Outline each uninfected red blood cell.
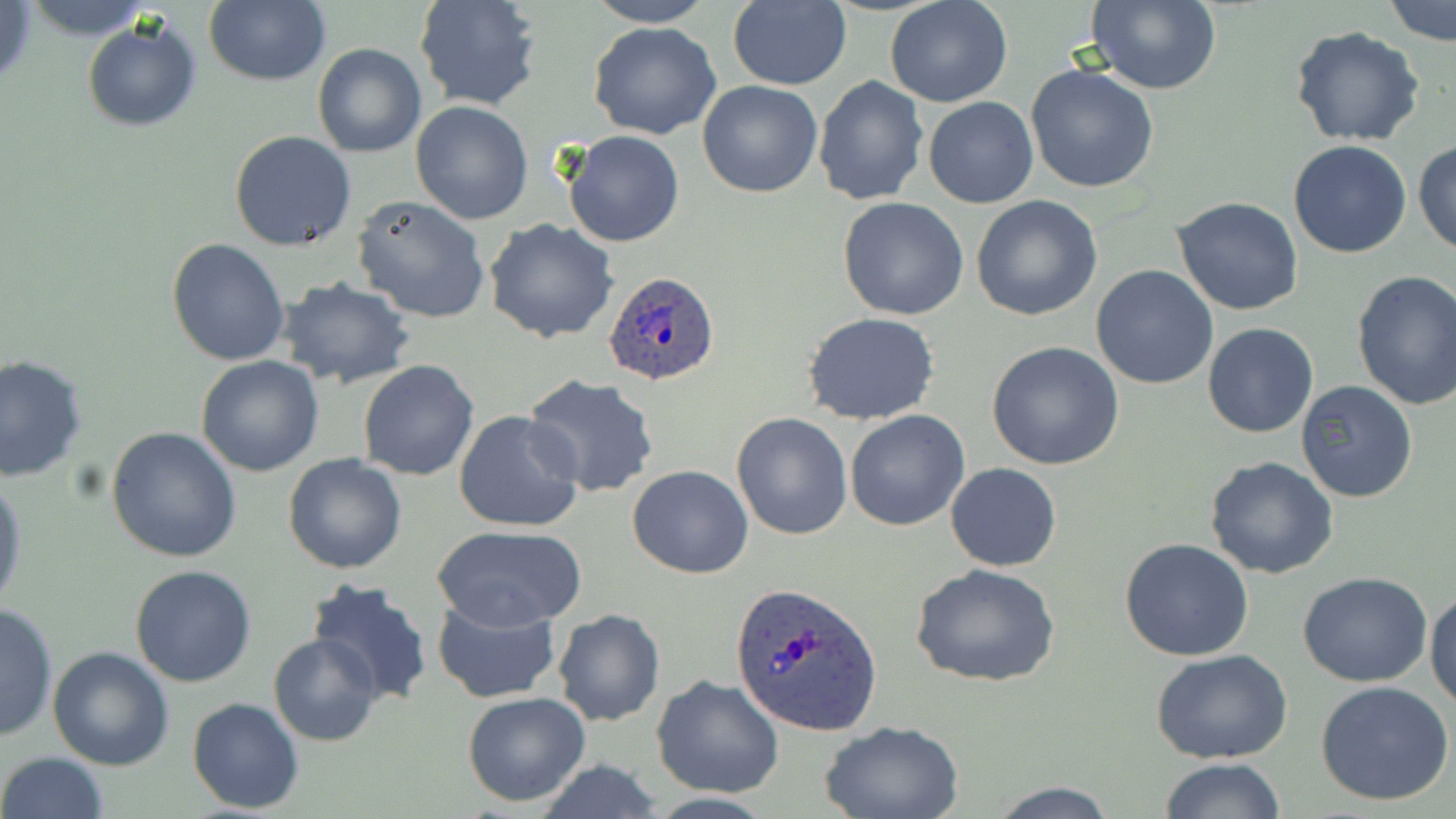
Approximate bounding boxes as (x1,y1)-(x2,y2) corner pairs in pixels.
Uninfected red blood cells: (204,0)-(330,87), (414,0)-(545,113), (584,0)-(716,26), (886,0)-(1013,107), (1384,0)-(1456,46), (725,1)-(852,89), (1086,1)-(1223,94), (0,2)-(38,90), (80,18)-(202,132), (587,20)-(722,140), (1289,26)-(1428,149), (312,43)-(426,158), (1025,63)-(1160,194), (813,74)-(928,207), (697,81)-(824,198), (922,96)-(1038,209), (409,100)-(533,224), (228,129)-(356,251), (563,129)-(686,247), (1288,140)-(1413,258), (1413,140)-(1456,257), (352,195)-(491,324), (971,195)-(1103,321), (837,197)-(969,321), (1172,197)-(1304,316), (485,219)-(619,342), (167,239)-(290,366), (1091,265)-(1219,390), (1351,270)-(1456,412), (276,275)-(416,390), (803,313)-(941,425), (1202,322)-(1319,438), (986,341)-(1127,470), (0,354)-(89,483), (196,355)-(324,476), (357,359)-(481,480), (523,375)-(659,497), (1295,379)-(1419,502), (454,410)-(584,533), (844,410)-(970,531), (731,412)-(853,540), (106,426)-(241,563), (283,453)-(409,574), (1204,455)-(1339,579), (945,464)-(1061,571), (628,465)-(754,578), (0,472)-(26,615), (433,524)-(587,630), (1120,536)-(1254,661), (910,562)-(1061,688), (130,563)-(257,686), (1297,571)-(1433,687), (303,576)-(434,706), (1426,587)-(1456,712), (430,595)-(562,704), (0,601)-(58,743), (553,609)-(666,727), (268,633)-(382,746), (48,645)-(175,770), (1151,648)-(1294,763), (652,674)-(784,798), (1314,680)-(1456,807), (463,692)-(591,807), (188,697)-(305,814), (821,720)-(964,819), (0,751)-(109,819), (1160,756)-(1287,819), (530,760)-(669,819), (982,780)-(1121,816).

Plasmodium ovale-infected red blood cell locations: (603,271)-(723,385), (729,582)-(882,735). Slide-level diagnosis: Plasmodium ovale. 1000x magnification. Optical microscopy. Image is 1456×819 pixels. One field of a larger specimen. Thin blood smear. May-Grünwald-Giemsa-stained preparation.